Comment on the morphology of the red blood cells.
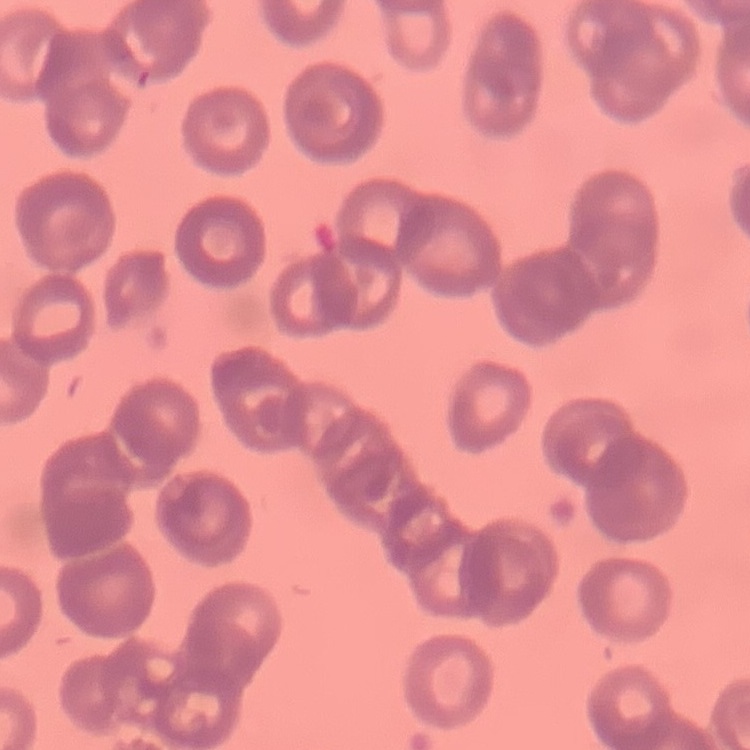
Rouleaux formation.

One tile cut from a larger photomicrograph. Stained with either Field's or Giemsa. Thin blood film.